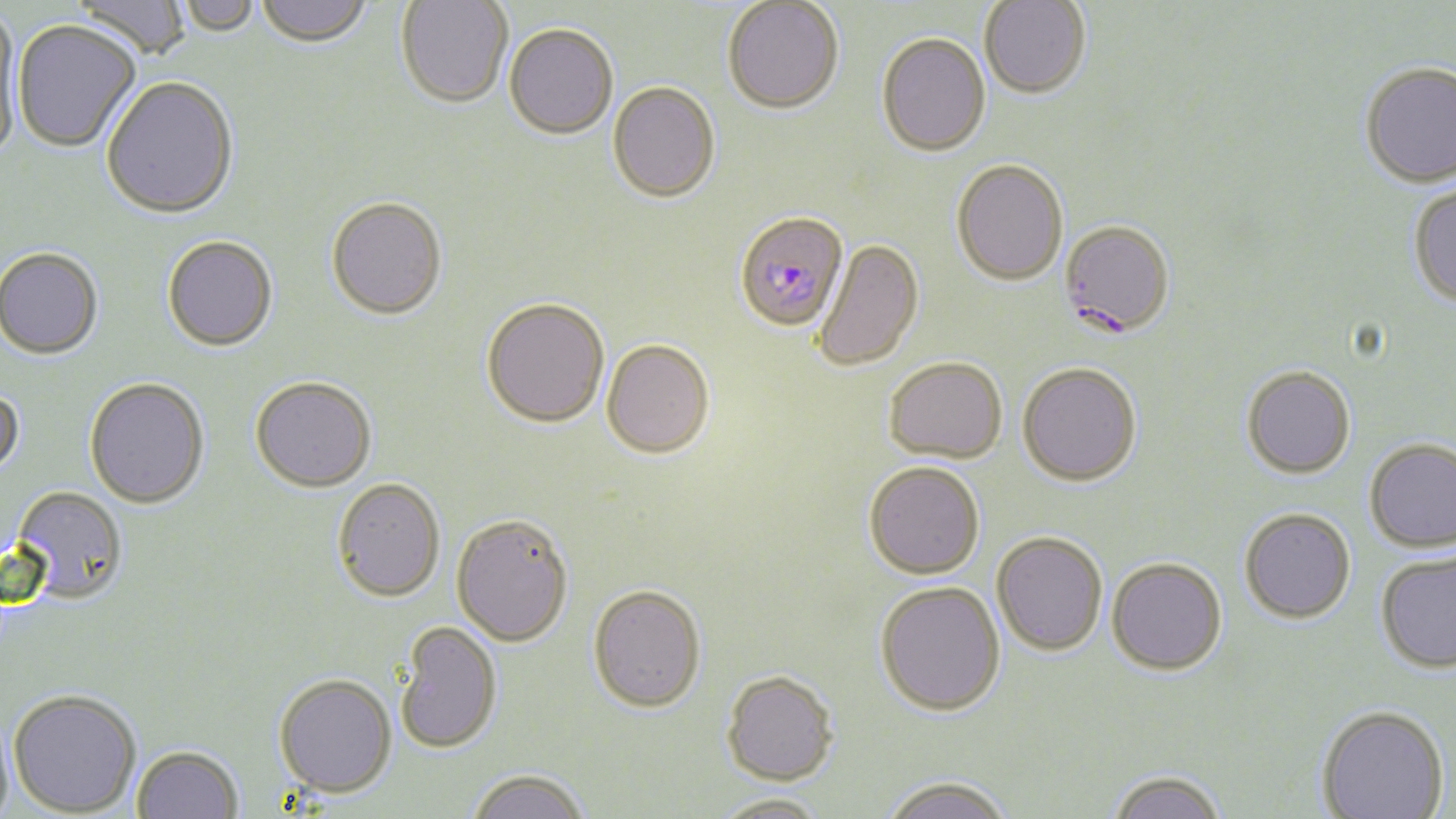

Summary:
  - Coordinate format: approximate bounding boxes as [x1, y1, x2, y2] in pixels
  - Uninfected red blood cell locations: [70, 0, 193, 62], [254, 0, 375, 49], [396, 0, 513, 109], [979, 0, 1091, 99], [174, 1, 262, 37], [722, 1, 844, 114], [0, 10, 24, 165], [11, 20, 142, 154], [504, 23, 618, 138], [877, 31, 991, 156], [1359, 61, 1456, 187], [100, 78, 239, 220], [608, 81, 720, 201], [951, 158, 1068, 285], [1407, 183, 1456, 308], [326, 198, 447, 322], [162, 236, 278, 353], [814, 239, 923, 371], [0, 248, 103, 361], [481, 297, 610, 428], [602, 339, 715, 458], [883, 357, 1007, 464], [1018, 361, 1142, 486], [1241, 365, 1356, 479], [250, 377, 377, 492], [84, 378, 210, 509], [0, 386, 25, 481], [1364, 437, 1456, 552], [863, 461, 985, 579], [332, 478, 446, 602], [10, 485, 128, 604], [1240, 507, 1356, 622], [451, 513, 573, 647], [992, 531, 1107, 656], [1375, 549, 1456, 673], [1107, 557, 1227, 675], [875, 580, 1006, 716], [588, 583, 707, 712], [395, 621, 503, 754], [721, 670, 838, 785], [273, 674, 397, 799], [8, 688, 141, 816], [1317, 704, 1450, 818], [132, 745, 244, 819], [466, 769, 591, 819], [1107, 769, 1227, 819], [880, 776, 1014, 819], [712, 793, 831, 819]
  - Plasmodium falciparum-infected red blood cell locations: [734, 210, 849, 331], [1059, 219, 1175, 338]
  - Slide-level diagnosis: Plasmodium falciparum
  - Magnification: 1000x
  - Stain: May-Grünwald-Giemsa
  - Modality: optical microscopy
  - Preparation: thin blood smear
  - Image size: 1456×819 pixels
  - Field of view: one of a larger specimen